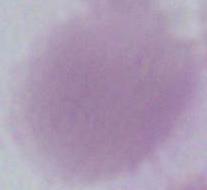

Captured at 1000x magnification. Micrograph. A red blood cell is seen.